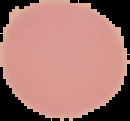

image type = segmented cell region with the area outside set to black
preparation = thin blood smear
image size = 130×121 pixels
malaria status = uninfected